Identify the parasite.
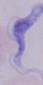

This is a trypanosome.

1000x magnification. Photomicrograph.